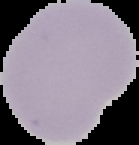
{
  "malaria_status": "uninfected",
  "image_type": "cell region segmented out of the field of view; surrounding area masked to black",
  "image_size": "139×145 pixels",
  "preparation": "thin blood smear"
}